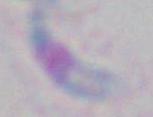
magnification = 1000x
identification = Toxoplasma gondii
modality = photomicrograph